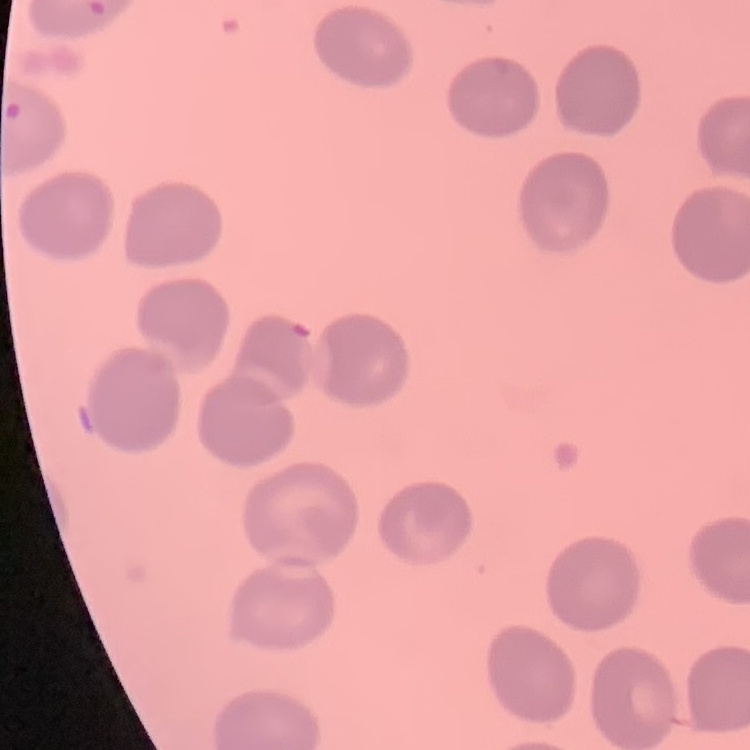
red blood cell morphology = no rouleaux formation
image type = square crop of a larger photomicrograph
preparation = thin blood smear
stain = Field's or Giemsa